Mark where cells are.
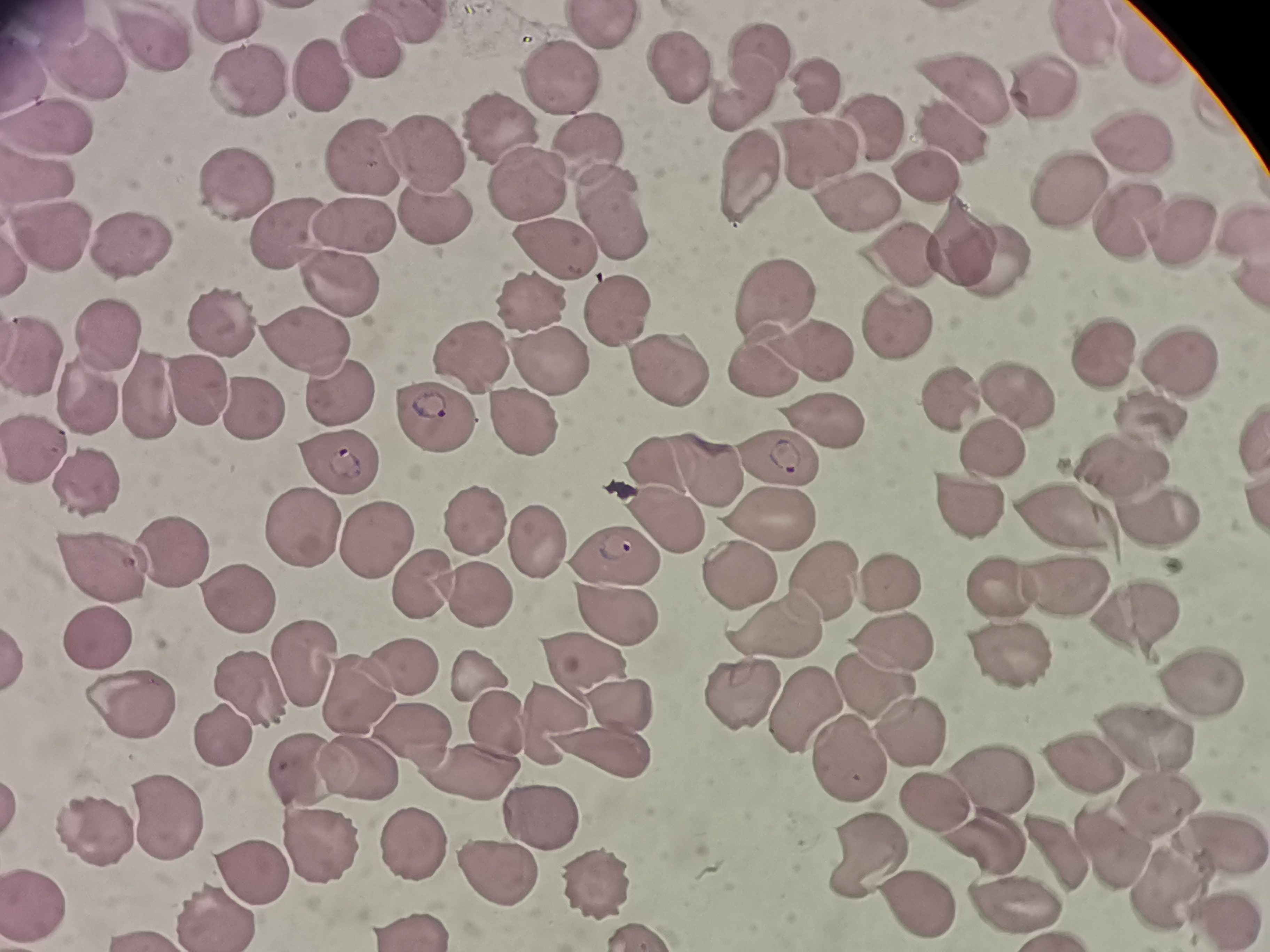
Approximate centers as (x, y) in pixels.
Cells: (234, 21), (598, 29), (1081, 36), (156, 42), (376, 47), (1149, 48), (760, 53), (86, 61), (675, 64), (318, 80), (561, 80), (247, 81), (818, 87), (968, 89), (1039, 91), (742, 102), (46, 123), (872, 126), (952, 130), (503, 135), (586, 147), (1128, 151), (429, 154), (367, 163), (814, 163), (740, 175), (932, 177), (233, 180), (1066, 186), (526, 193), (860, 205), (613, 208), (433, 218), (1122, 221), (1241, 224), (355, 229), (282, 234), (1177, 239), (49, 242), (557, 244), (955, 249), (132, 253), (902, 255), (982, 259), (343, 279), (785, 296), (613, 306), (526, 308), (223, 332), (898, 332), (102, 334), (309, 343), (35, 349), (474, 354), (1114, 355), (814, 356), (761, 362), (548, 365), (659, 366), (1179, 377), (1020, 391), (197, 393), (336, 394), (143, 398), (94, 399), (960, 400), (247, 414), (434, 417), (519, 423), (1143, 425), (823, 437), (36, 444), (989, 451), (336, 463), (661, 465), (1129, 466), (776, 467), (706, 472), (88, 486), (960, 501), (1154, 519), (467, 520), (665, 522), (774, 524), (1064, 524), (301, 535), (375, 538), (533, 543), (173, 554), (619, 554), (103, 563), (817, 576), (731, 577), (890, 581), (417, 583), (1007, 591), (1071, 594), (239, 597), (472, 600), (615, 607), (1135, 624), (776, 625), (92, 636), (897, 640), (1004, 656), (587, 663), (306, 665), (409, 674), (472, 680), (1198, 681), (871, 686), (256, 689), (360, 692), (733, 694), (623, 701), (809, 718), (125, 720), (553, 720), (497, 725), (907, 731), (409, 734), (1143, 734), (231, 739), (600, 751), (846, 761), (1079, 762), (308, 769), (357, 772), (466, 772), (999, 777), (929, 794), (1158, 804), (534, 811), (173, 820), (1223, 837), (983, 838), (104, 840), (324, 842), (865, 846), (1111, 849), (421, 850), (1056, 851), (500, 867), (256, 876), (596, 884), (1165, 890), (1008, 897), (912, 902), (216, 915).

Summary:
  - Field of view: single
  - Capture: smartphone camera at the microscope eyepiece
  - Image size: 1270×952 pixels
  - Preparation: thin blood smear
  - Stain: Giemsa